Locate every blood parasite and identify its species.
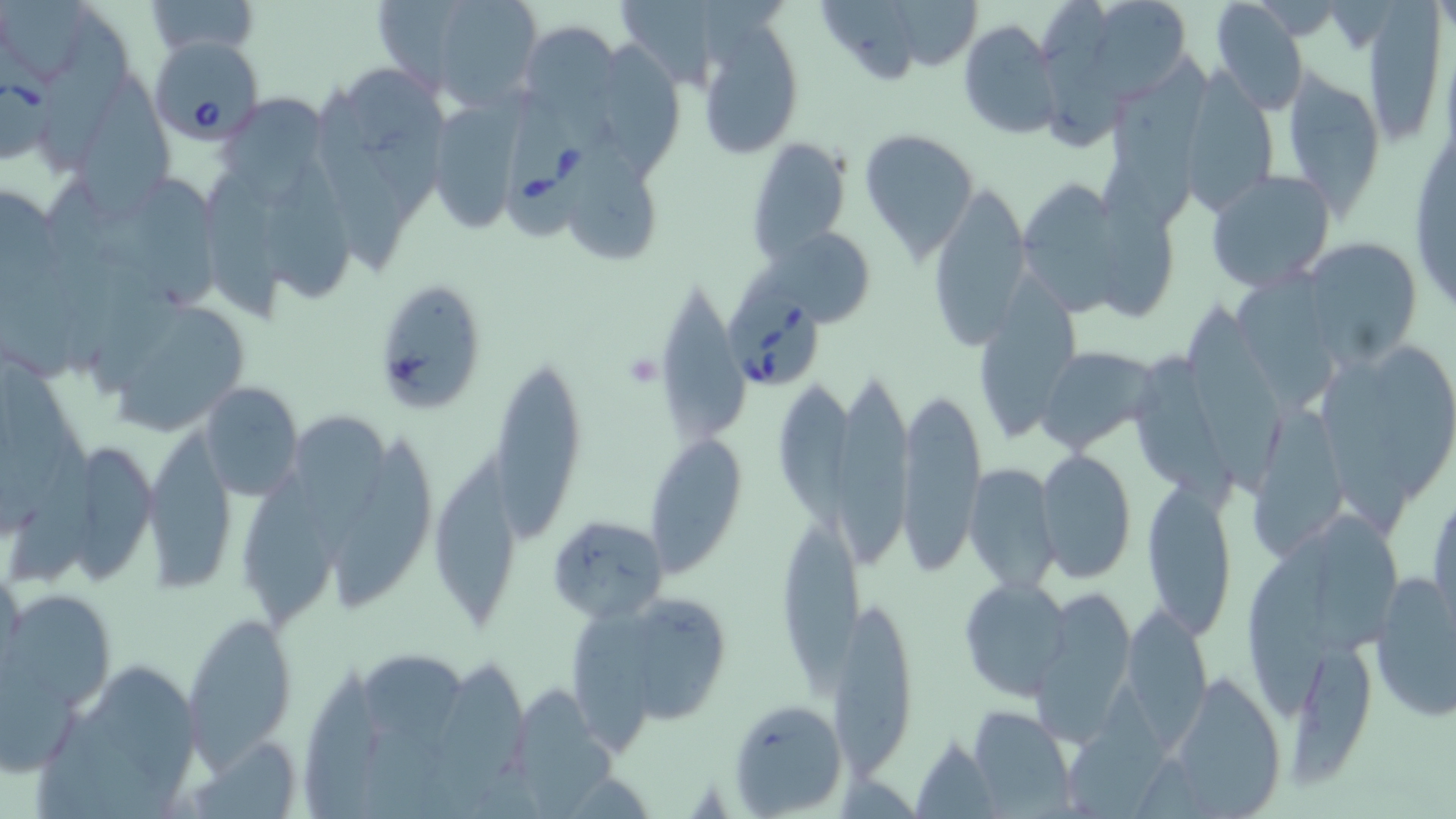
Approximate bounding boxes as (x1, y1, x2, y2) in pixels.
Babesia divergens-infected red blood cells: (151, 34, 265, 147), (0, 72, 56, 167), (500, 103, 604, 240), (726, 292, 827, 393).
No Plasmodium falciparum, Plasmodium ovale, Plasmodium malariae, Plasmodium vivax, or Trypanosoma brucei observed.

slide-level diagnosis = Babesia divergens
field of view = one of a larger specimen
modality = optical microscopy
platelet locations = approximate bounding boxes as (x1, y1, x2, y2) in pixels: (623, 352, 662, 389)
image size = 1456×819 pixels
magnification = 1000x
preparation = thin blood film
stain = May-Grünwald-Giemsa
uninfected red blood cell locations = approximate bounding boxes as (x1, y1, x2, y2) in pixels: (144, 0, 260, 57), (425, 0, 544, 109), (824, 0, 922, 89), (1209, 0, 1308, 114), (894, 1, 987, 72), (1037, 1, 1137, 155), (0, 3, 104, 90), (624, 4, 720, 93), (1085, 4, 1197, 108), (1361, 9, 1448, 139), (517, 18, 621, 121), (697, 18, 806, 161), (957, 21, 1061, 139), (599, 39, 691, 179), (1110, 50, 1214, 223), (345, 64, 453, 227), (1285, 70, 1384, 213), (81, 75, 185, 223), (1179, 76, 1276, 216), (313, 88, 409, 269), (222, 97, 338, 209), (434, 98, 532, 238), (1407, 111, 1454, 324), (860, 127, 979, 260), (574, 136, 667, 262), (746, 137, 852, 261), (270, 161, 356, 304), (1087, 161, 1178, 321), (1203, 168, 1337, 292), (202, 173, 292, 332), (1011, 175, 1128, 324), (1, 180, 65, 308), (138, 182, 228, 312), (926, 182, 1030, 348), (770, 224, 877, 328), (1302, 239, 1421, 362), (973, 272, 1083, 445), (1231, 272, 1338, 412), (653, 274, 749, 448), (374, 283, 492, 415), (96, 294, 254, 436), (1184, 311, 1288, 495), (1033, 345, 1156, 453), (1376, 345, 1452, 501), (1131, 348, 1242, 514), (490, 354, 585, 533), (1323, 366, 1414, 541), (195, 379, 305, 500), (835, 379, 918, 575), (771, 382, 874, 541), (897, 384, 985, 574), (1245, 405, 1354, 557), (291, 416, 401, 564), (144, 430, 239, 588), (645, 431, 748, 574), (327, 432, 439, 611), (65, 439, 160, 574), (1033, 449, 1136, 582), (438, 451, 525, 633), (235, 459, 339, 640), (965, 463, 1060, 593), (1429, 475, 1456, 633), (1140, 477, 1238, 637), (547, 515, 670, 623), (1313, 515, 1408, 658), (778, 523, 866, 702), (1241, 533, 1348, 717), (0, 564, 26, 679), (1370, 571, 1456, 722), (958, 579, 1070, 700), (1031, 586, 1138, 738), (5, 589, 116, 712), (833, 594, 919, 775), (632, 595, 733, 730), (1122, 604, 1212, 745), (567, 609, 665, 758), (180, 611, 300, 769), (1284, 640, 1375, 786), (360, 647, 476, 792), (0, 654, 86, 776), (39, 656, 208, 813), (1162, 672, 1287, 814), (1059, 686, 1178, 817), (730, 699, 847, 816), (967, 705, 1076, 814), (912, 734, 1002, 815)